Locate every Plasmodium parasite.
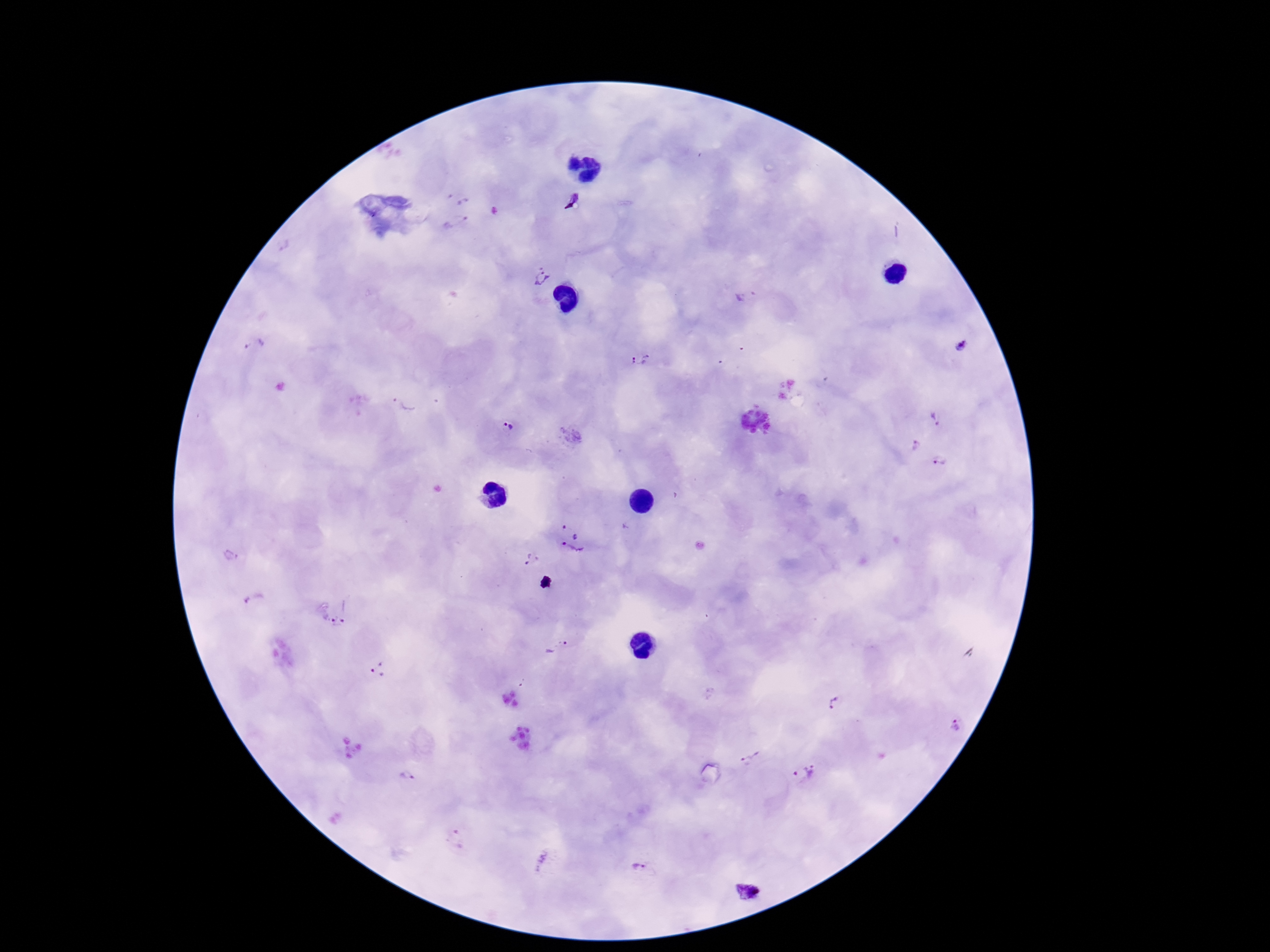

Approximate object centers, in pixels from the top-left corner.
Plasmodium parasites: (x=462, y=197), (x=568, y=198), (x=455, y=222), (x=543, y=277), (x=745, y=295), (x=255, y=344), (x=962, y=344), (x=641, y=359), (x=402, y=401), (x=935, y=417), (x=508, y=426), (x=916, y=445), (x=940, y=461), (x=570, y=527), (x=572, y=552), (x=530, y=559), (x=254, y=600), (x=338, y=615), (x=557, y=646), (x=380, y=669), (x=834, y=704), (x=957, y=725), (x=749, y=756), (x=804, y=772), (x=407, y=774), (x=457, y=840), (x=639, y=868), (x=750, y=892).

capture = smartphone camera through the microscope eyepiece
preparation = thick blood smear
field of view = single
image size = 1270×952 pixels
magnification = 100x
stain = Giemsa
patient malaria status = infected